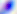
magnification = 400x
modality = photomicrograph
identification = Toxoplasma gondii